Assess the morphology of the erythrocytes.
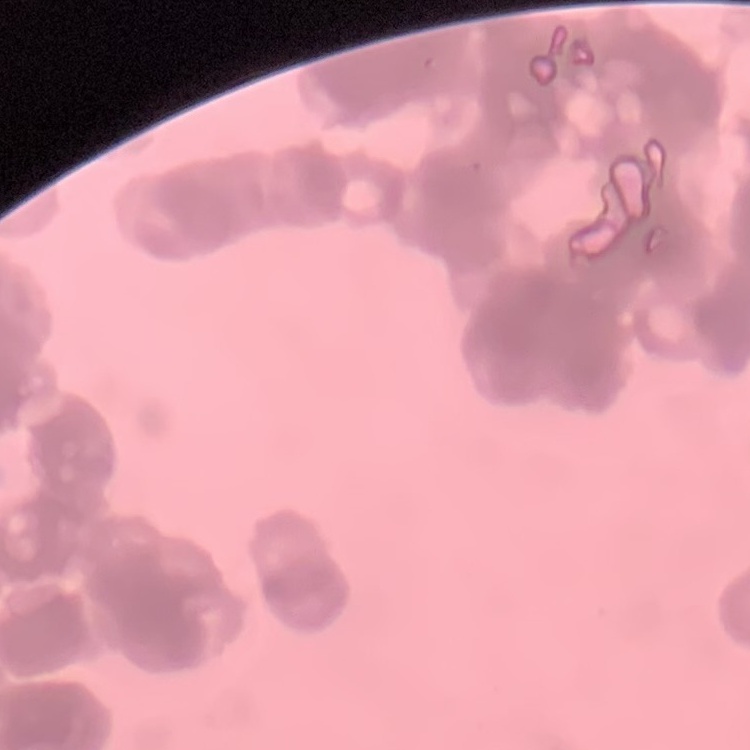

They show rouleaux formation.

Stained with either Field's or Giemsa. One tile cut from a larger photomicrograph. Thin blood film.